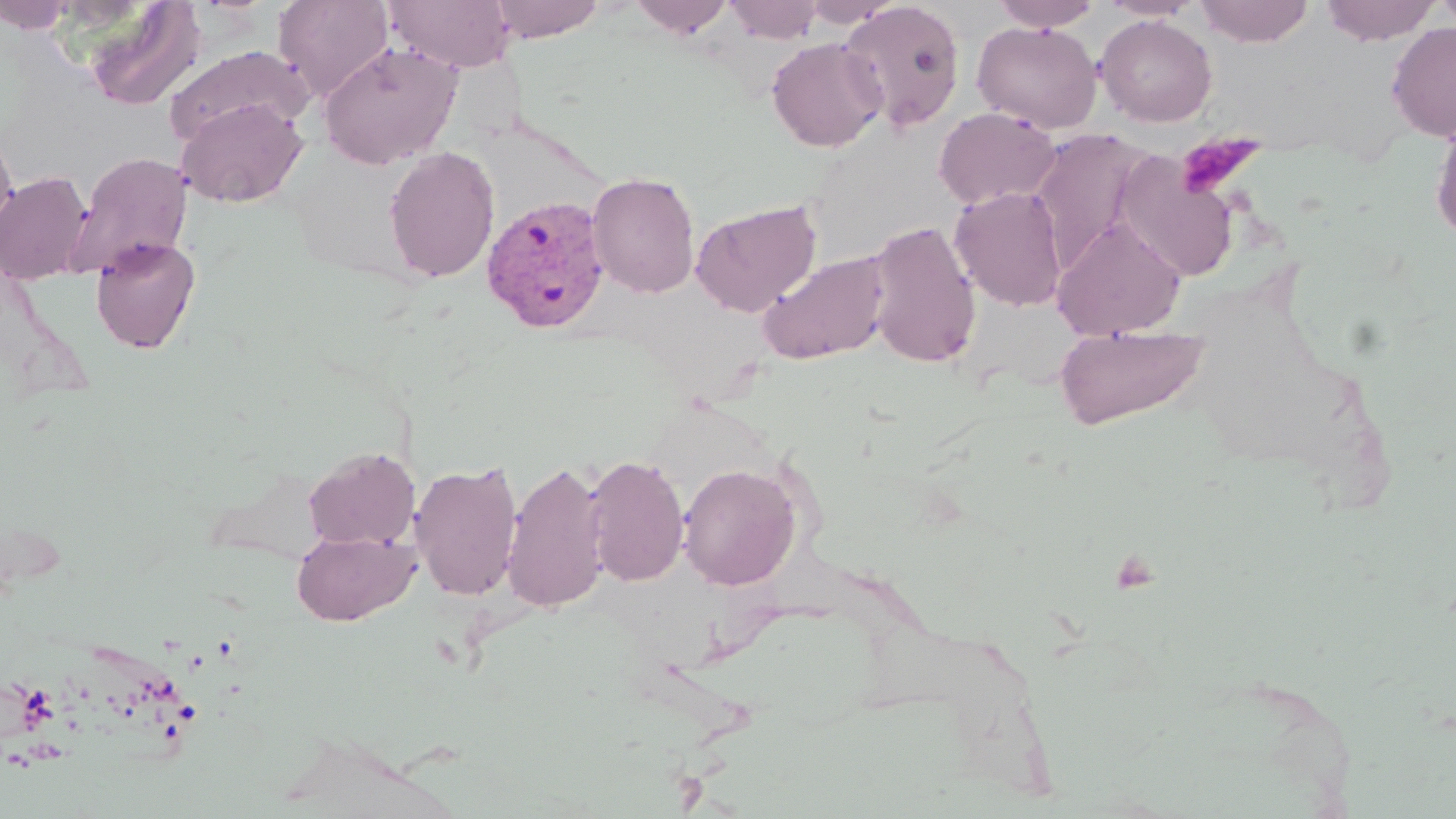 Approximate bounding boxes as (x1,y1)-(x2,y2) corner pairs in pixels. Plasmodium vivax-infected red blood cell locations: (481,194)-(611,334). Uninfected red blood cell locations: (0,0)-(75,33), (273,0)-(393,102), (486,0)-(606,42), (630,0)-(733,38), (799,0)-(904,28), (991,0)-(1101,30), (1100,0)-(1202,20), (1194,0)-(1314,47), (1319,0)-(1441,45), (1433,0)-(1456,36), (82,1)-(208,110), (385,1)-(516,72), (723,1)-(823,43), (839,1)-(967,132), (1096,15)-(1218,127), (972,20)-(1102,134), (1386,22)-(1456,141), (767,37)-(886,151), (318,41)-(464,169), (163,44)-(311,149), (177,97)-(307,208), (933,106)-(1060,210), (1430,114)-(1456,245), (0,123)-(17,239), (383,145)-(500,283), (67,150)-(193,280), (1114,153)-(1242,282), (0,171)-(93,284), (587,171)-(700,299), (949,186)-(1068,311), (690,199)-(821,317), (1052,217)-(1187,340), (866,219)-(982,369), (90,237)-(201,354), (758,250)-(891,365), (1054,325)-(1210,430), (303,446)-(418,550), (584,453)-(690,588), (410,460)-(523,601), (502,460)-(610,613), (678,462)-(802,590), (291,528)-(420,625). Platelet locations: (1175,133)-(1266,198). Slide-level diagnosis: Plasmodium vivax. Light microscopy. Single field of view. Image is 1456×819 pixels. Captured at 1000x magnification. May-Grünwald-Giemsa-stained preparation. Thin blood smear.